Report the malaria status of this cell.
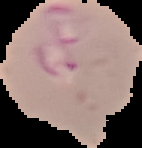

Parasitized.

The area outside the segmented cell region is set to black. Image is 142×148 pixels. From a thin blood smear.